Locate every Plasmodium parasite.
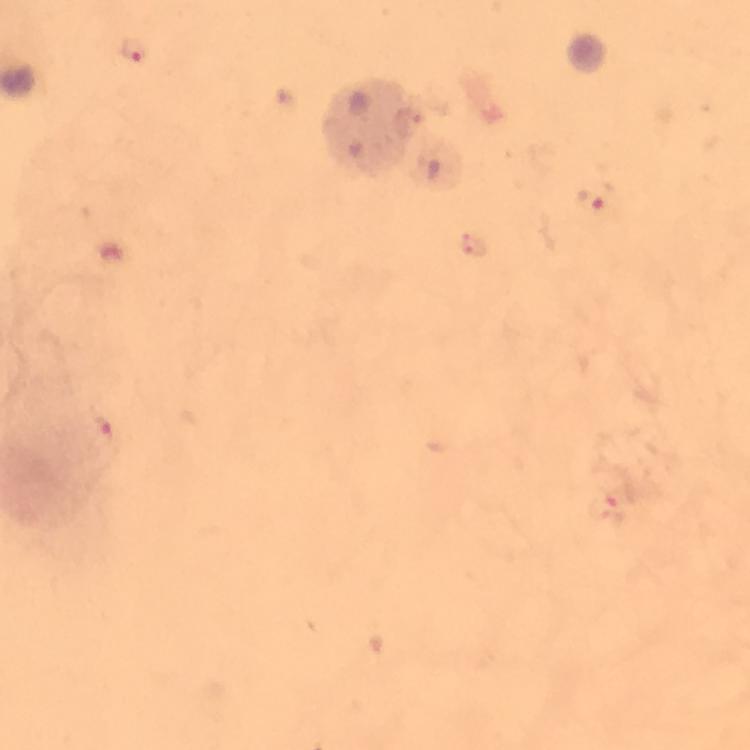
Approximate object centers, in pixels from the top-left corner.
Plasmodium parasites: (x=133, y=51), (x=590, y=203), (x=103, y=429), (x=607, y=508).

preparation = thick blood smear
magnification = 100x
immersion oil = applied
stain = Giemsa
image size = 750×750 pixels
capture = smartphone mounted on the microscope
context = from a diagnostic examination for malaria
cropped from = a single field of view